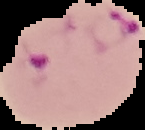
From a thin blood film. Cell region segmented out of the field of view; the surrounding area is masked to black. Malaria status: parasitized. Image is 145×130 pixels.